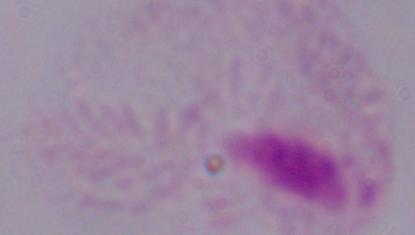 1000x magnification. Photomicrograph. A trichomonad is shown.